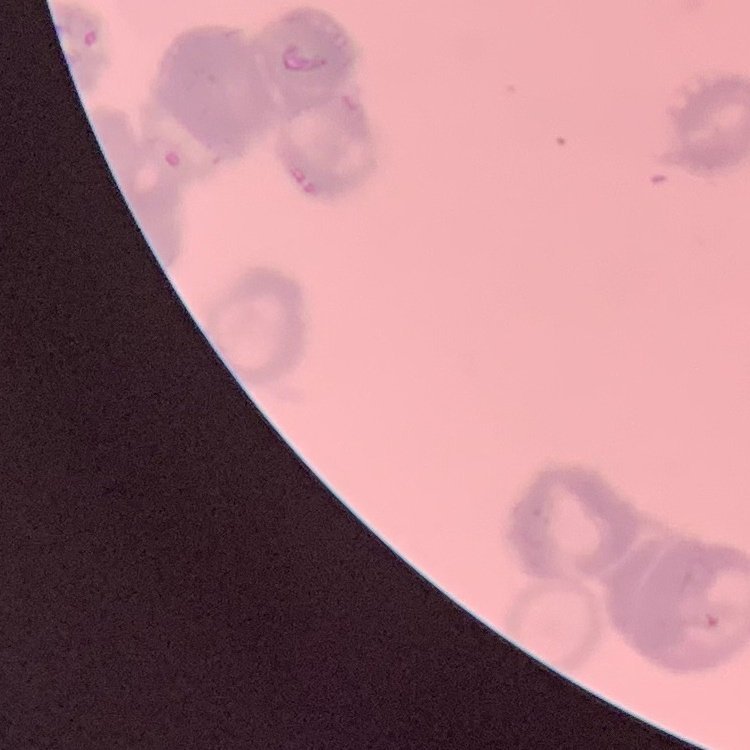
The red blood cells exhibit rouleaux formation. One tile cut from a larger photomicrograph. Thin blood film. Field's or Giemsa stain.